Locate every Plasmodium falciparum-infected red blood cell.
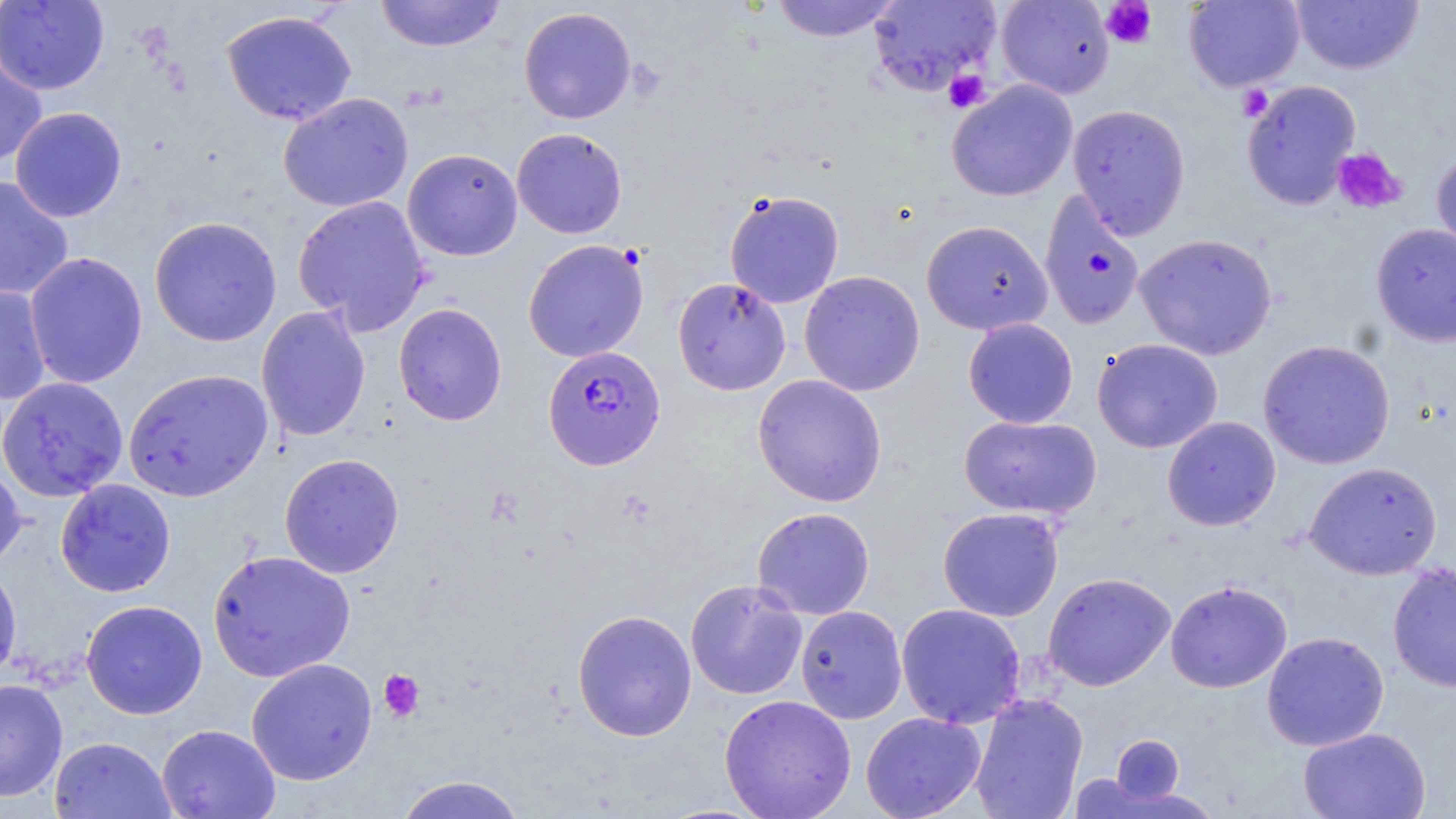
Approximate bounding boxes as (x1,y1)-(x2,y2) corner pairs in pixels.
Plasmodium falciparum-infected red blood cells: (542,345)-(665,469).

Uninfected red blood cell locations: (0,0)-(110,95), (374,0)-(506,52), (768,0)-(903,42), (869,0)-(1002,97), (995,0)-(1116,100), (1183,0)-(1304,92), (1290,1)-(1424,74), (518,6)-(637,124), (221,9)-(358,125), (0,46)-(48,168), (1241,79)-(1361,211), (947,80)-(1078,202), (278,92)-(414,213), (1067,103)-(1191,239), (10,106)-(127,222), (512,127)-(628,239), (1431,146)-(1456,262), (403,149)-(523,261), (0,175)-(74,302), (724,189)-(844,308), (1039,190)-(1145,331), (292,196)-(431,335), (149,216)-(282,347), (921,220)-(1052,335), (1371,223)-(1456,346), (1134,232)-(1278,360), (522,239)-(649,362), (24,252)-(148,389), (799,270)-(926,396), (672,277)-(791,395), (0,284)-(51,405), (393,303)-(507,426), (256,306)-(371,442), (962,318)-(1078,428), (1092,338)-(1223,453), (1258,339)-(1396,469), (123,368)-(273,502), (752,374)-(888,507), (0,376)-(129,502), (959,415)-(1102,519), (1162,416)-(1281,531), (279,453)-(405,578), (0,458)-(26,573), (1304,461)-(1443,580), (55,479)-(176,597), (69,480)-(184,719), (751,506)-(876,620), (937,507)-(1064,622), (206,549)-(356,683), (0,559)-(23,687), (1387,562)-(1456,692), (1042,572)-(1176,691), (685,579)-(808,700), (1165,580)-(1292,693), (81,599)-(208,719), (896,603)-(1026,728), (795,605)-(908,724), (572,609)-(697,742), (1261,631)-(1389,751), (245,658)-(378,785), (0,678)-(68,802), (969,692)-(1088,819), (719,694)-(857,819), (860,711)-(986,819), (156,724)-(281,819), (1298,726)-(1431,818), (1111,734)-(1185,805), (49,736)-(176,819), (393,774)-(529,819). Platelet locations: (1100,1)-(1157,49), (942,69)-(990,113), (1237,85)-(1274,122), (1332,147)-(1406,213), (378,669)-(425,723). Slide-level diagnosis: Plasmodium falciparum. Captured at 1000x magnification. May-Grünwald-Giemsa stain. Thin blood film. Light microscopy. Single field of view. Image is 1456×819 pixels.